Report the malaria status of this cell.
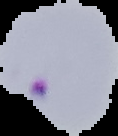

Parasitized.

From a thin blood smear. Segmented cell region on a black background. Image is 118×136 pixels.